Locate every Plasmodium parasite.
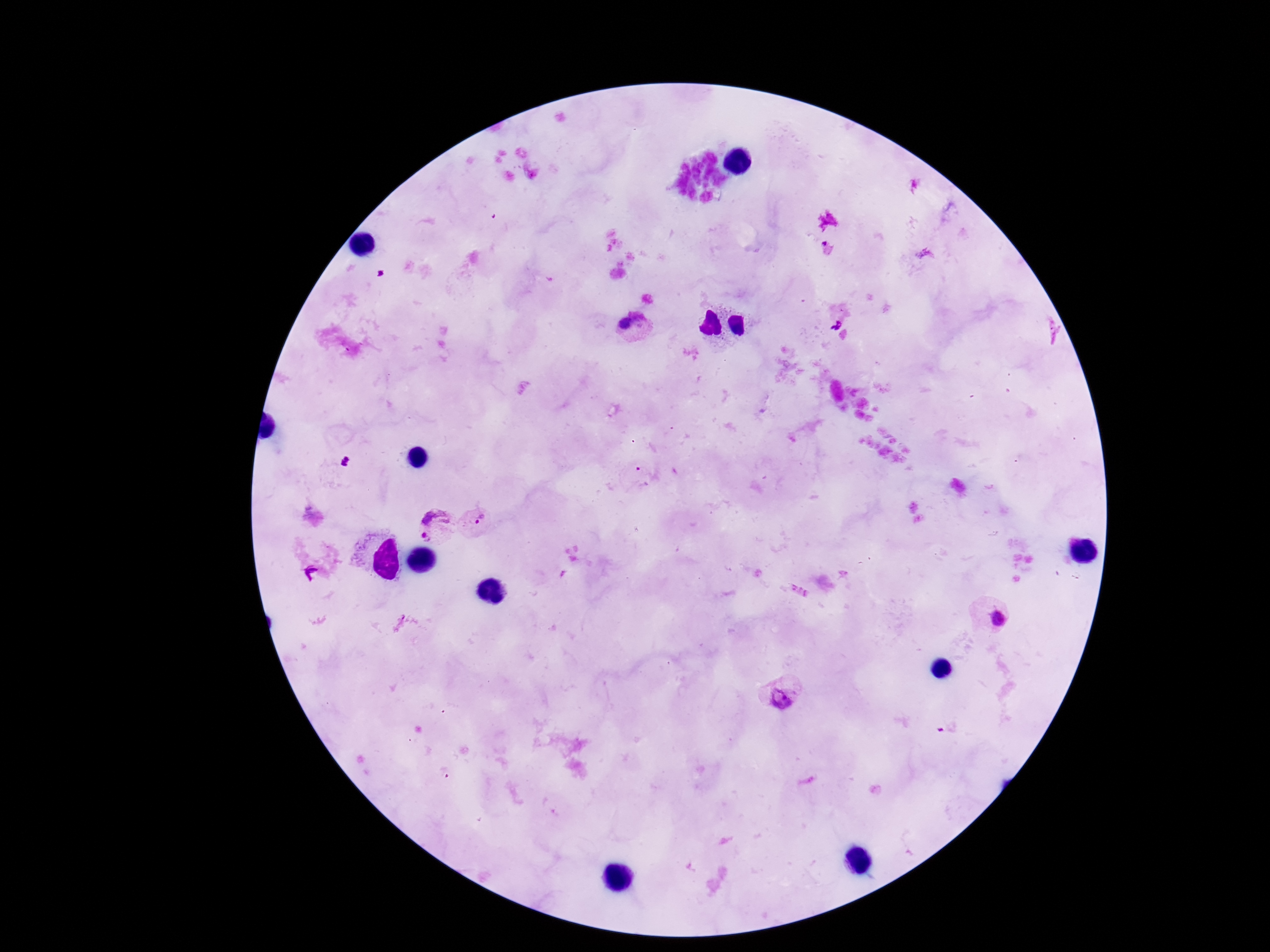
Approximate object centers, in pixels from the top-left corner.
Plasmodium parasites: (x=835, y=323), (x=632, y=327), (x=480, y=522), (x=432, y=525), (x=990, y=615), (x=782, y=697).

preparation = thick blood smear
capture = smartphone camera through the microscope eyepiece
image size = 1270×952 pixels
field of view = one from this slide
magnification = 100x
patient malaria status = positive
stain = Giemsa